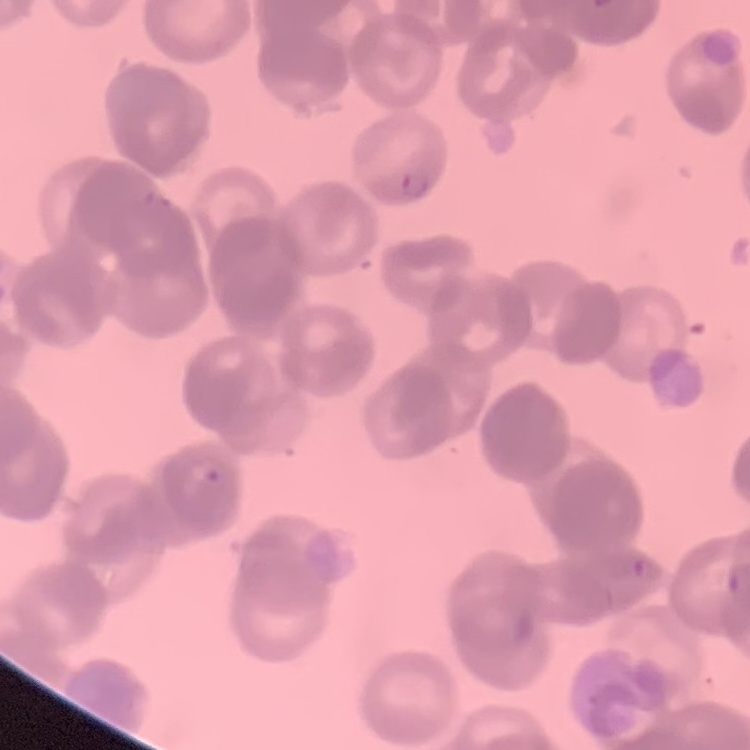

red blood cell morphology = rouleaux formation
stain = Field's or Giemsa
preparation = thin blood film
image type = one tile cut from a larger photomicrograph